Report the malaria status of this cell.
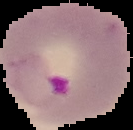
Parasitized.

preparation: thin blood film
image_size: 133×130 pixels
image_type: segmented cell region with the area outside set to black